Describe the morphology of the red blood cells.
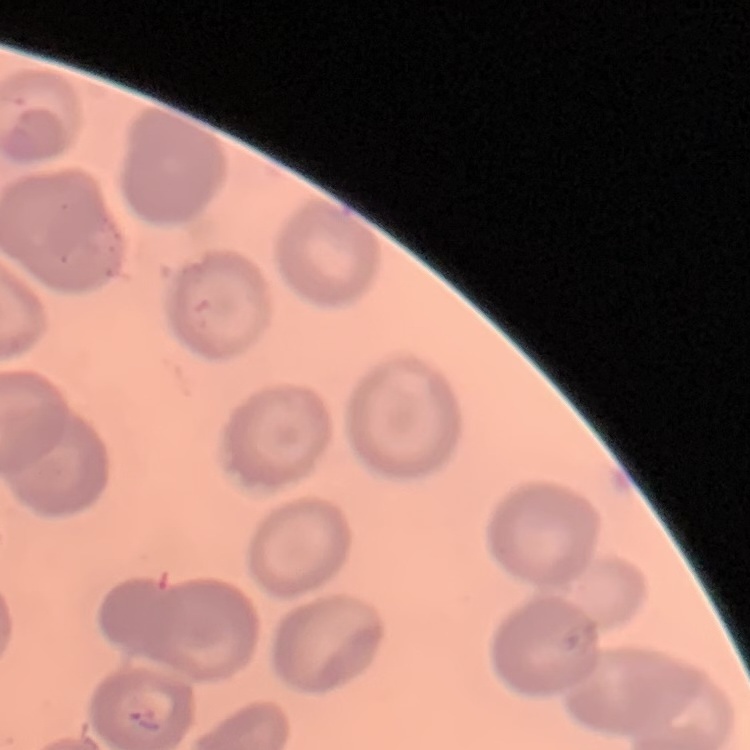

They show no rouleaux formation.

Summary:
  - Preparation: thin blood film
  - Stain: Field's or Giemsa
  - Image type: one tile cut from a larger photomicrograph